Report the malaria status of this cell.
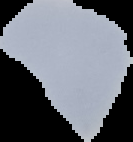

It is uninfected.

image type = cell region segmented out of the field of view; surrounding area masked to black
image size = 133×142 pixels
preparation = thin blood film